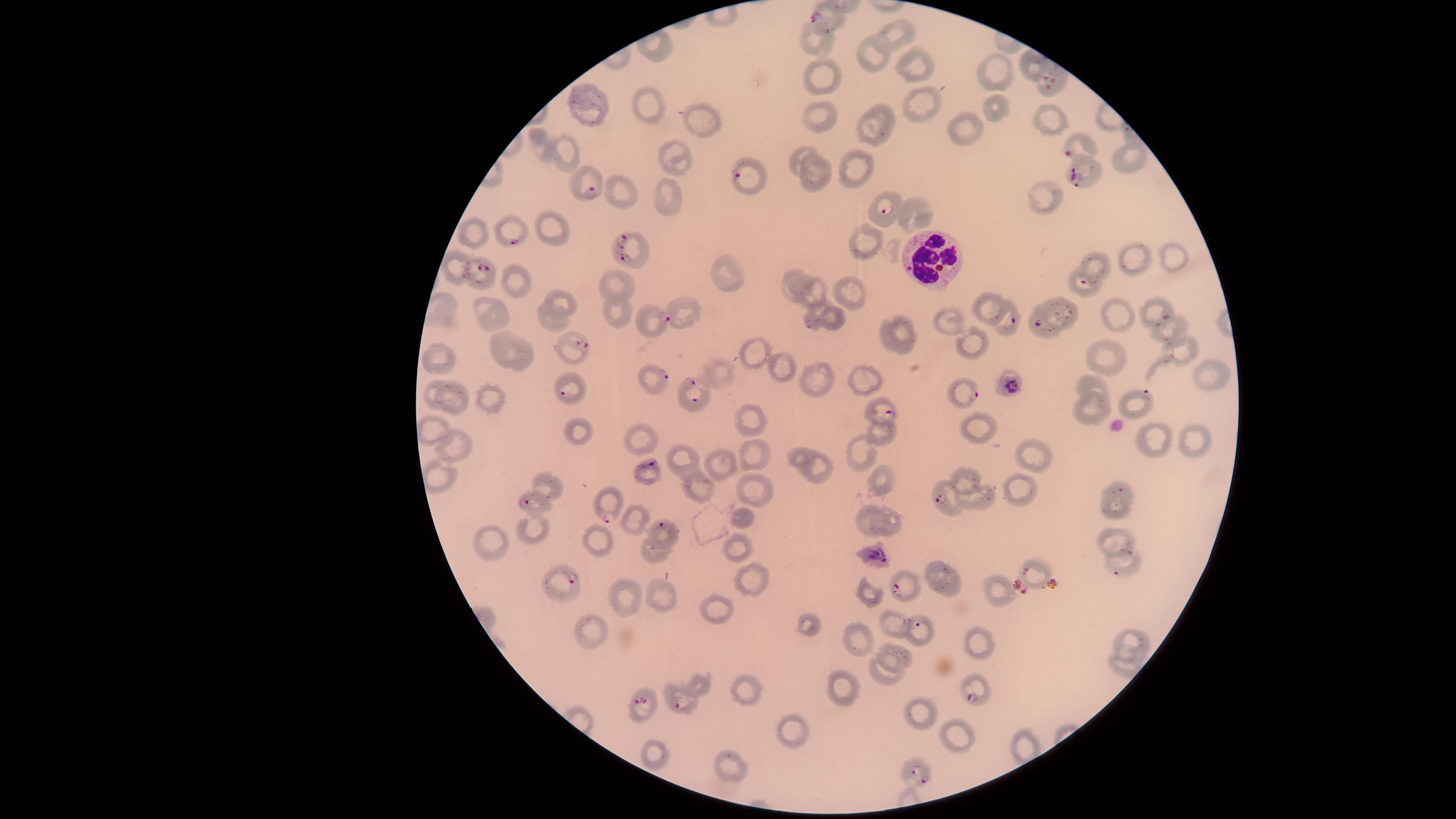

Approximate marker points as [x, y] in pixels.
Summary:
  - Uninfected red blood cells: [898, 36], [823, 41], [872, 55], [919, 68], [997, 70], [822, 74], [922, 96], [649, 105], [594, 107], [1000, 110], [822, 113], [1051, 118], [700, 121], [881, 123], [965, 128], [565, 149], [802, 154], [680, 156], [1132, 165], [862, 166], [822, 175], [621, 192], [663, 197], [1047, 198], [923, 215], [554, 229], [478, 232], [870, 240], [1176, 259], [1135, 260], [458, 263], [1097, 265], [725, 273], [796, 275], [519, 281], [853, 288], [619, 290], [815, 291], [562, 297], [989, 303], [495, 310], [817, 310], [1065, 311], [617, 312], [1120, 314], [954, 318], [557, 322], [833, 323], [661, 325], [1174, 330], [902, 331], [505, 341], [982, 345], [1182, 348], [754, 356], [1108, 357], [443, 358], [526, 358], [784, 366], [1215, 367], [723, 372], [819, 373], [864, 373], [1097, 386], [431, 390], [456, 401], [491, 401], [1094, 406], [748, 418], [979, 425], [581, 429], [428, 430], [883, 432], [641, 438], [1156, 441], [461, 443], [1196, 443], [866, 450], [1038, 452], [798, 453], [755, 456], [681, 460], [718, 464], [819, 467], [964, 476], [885, 480], [698, 483], [552, 484], [1019, 488], [757, 489], [980, 498], [873, 515], [745, 518], [633, 521], [894, 526], [537, 533], [599, 540], [1117, 542], [488, 545], [740, 546], [653, 554], [746, 577], [942, 579], [665, 596], [870, 597], [1001, 597], [625, 602], [724, 614], [806, 625], [898, 628], [593, 630], [858, 636], [1134, 637], [985, 642], [898, 655], [890, 676], [845, 688], [744, 694], [917, 712], [792, 732], [956, 732], [659, 753], [731, 764]
  - Parasitized red blood cells: [825, 20], [1051, 84], [1072, 148], [745, 178], [1080, 180], [587, 186], [885, 212], [514, 234], [631, 253], [484, 271], [1083, 285], [1165, 318], [669, 321], [1009, 321], [1036, 326], [581, 346], [665, 378], [694, 384], [1014, 386], [566, 392], [971, 394], [1147, 394], [886, 410], [648, 464], [1121, 490], [945, 499], [526, 502], [606, 515], [662, 526], [876, 560], [1026, 571], [1115, 574], [572, 579], [897, 588], [918, 625], [971, 697], [644, 703], [678, 704], [919, 774]
  - White blood cells: [931, 256]
  - Capture: smartphone photograph through the microscope eyepiece
  - Presence: malaria parasites seen
  - Stain: Giemsa
  - Field of view: single
  - Visible region: circular
  - Species: Plasmodium falciparum
  - Preparation: thin smear of blood
  - Image size: 1456×819 pixels